Classify this cell by malaria status.
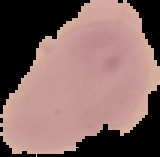

Uninfected.

{
  "preparation": "thin blood smear",
  "image_size": "160×157 pixels",
  "image_type": "segmented cell region on a black background"
}